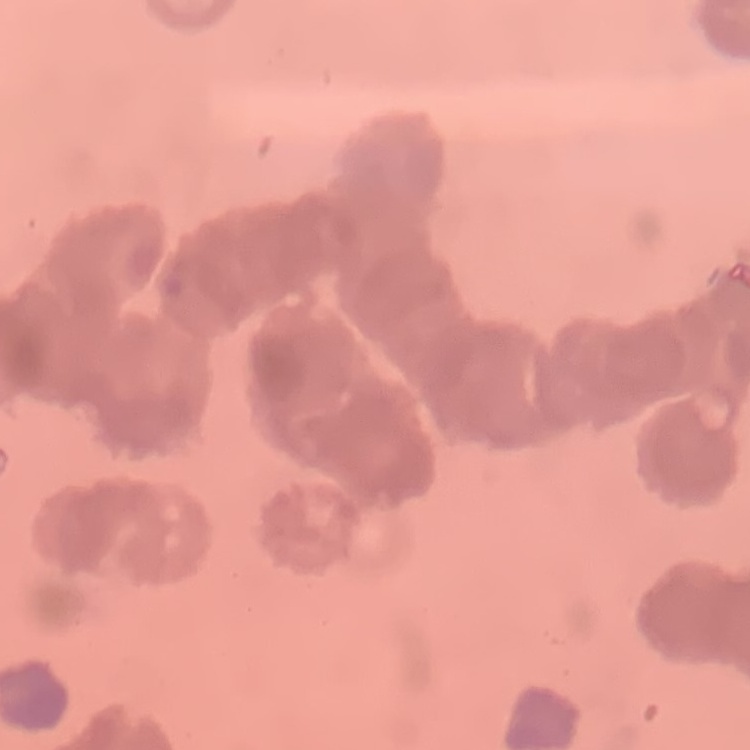
Summary:
  - Red blood cell morphology: rouleaux formation
  - Image type: square crop of a larger photomicrograph
  - Stain: Field's or Giemsa
  - Preparation: thin peripheral smear